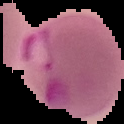
Malaria status: parasitized. Image is 124×124 pixels. Segmented cell region on a black background. From a thin blood film.